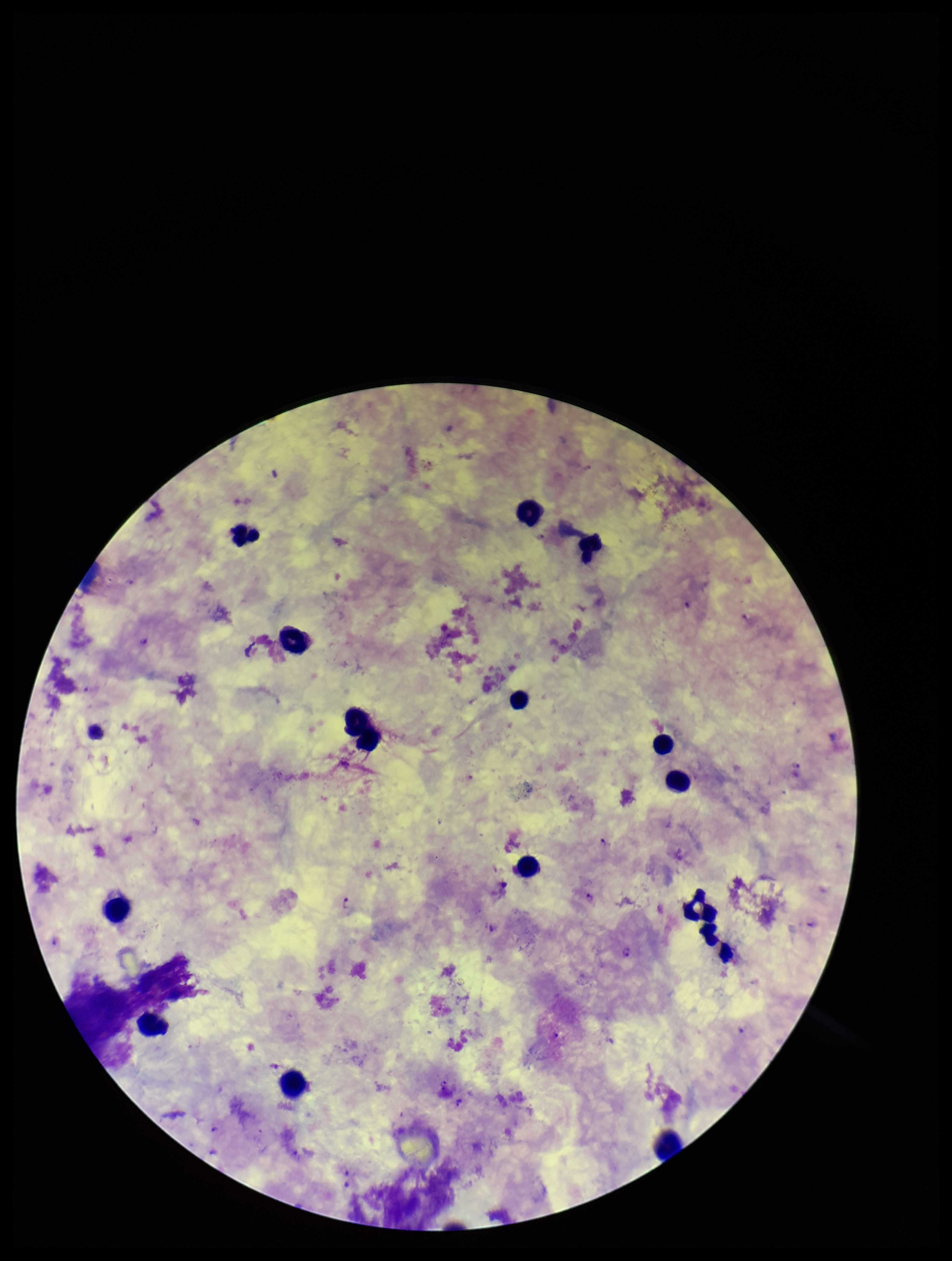

Summary:
  - Leukocyte count: 16
  - Patient malaria status: positive
  - Species reported for this patient: Plasmodium falciparum
  - Field of view: single
  - Parasite count: 5
  - Capture: smartphone photograph through the microscope eyepiece
  - Plasmodium parasites: detected
  - Preparation: thick blood smear
  - Stain: Giemsa
  - Image size: 952×1261 pixels